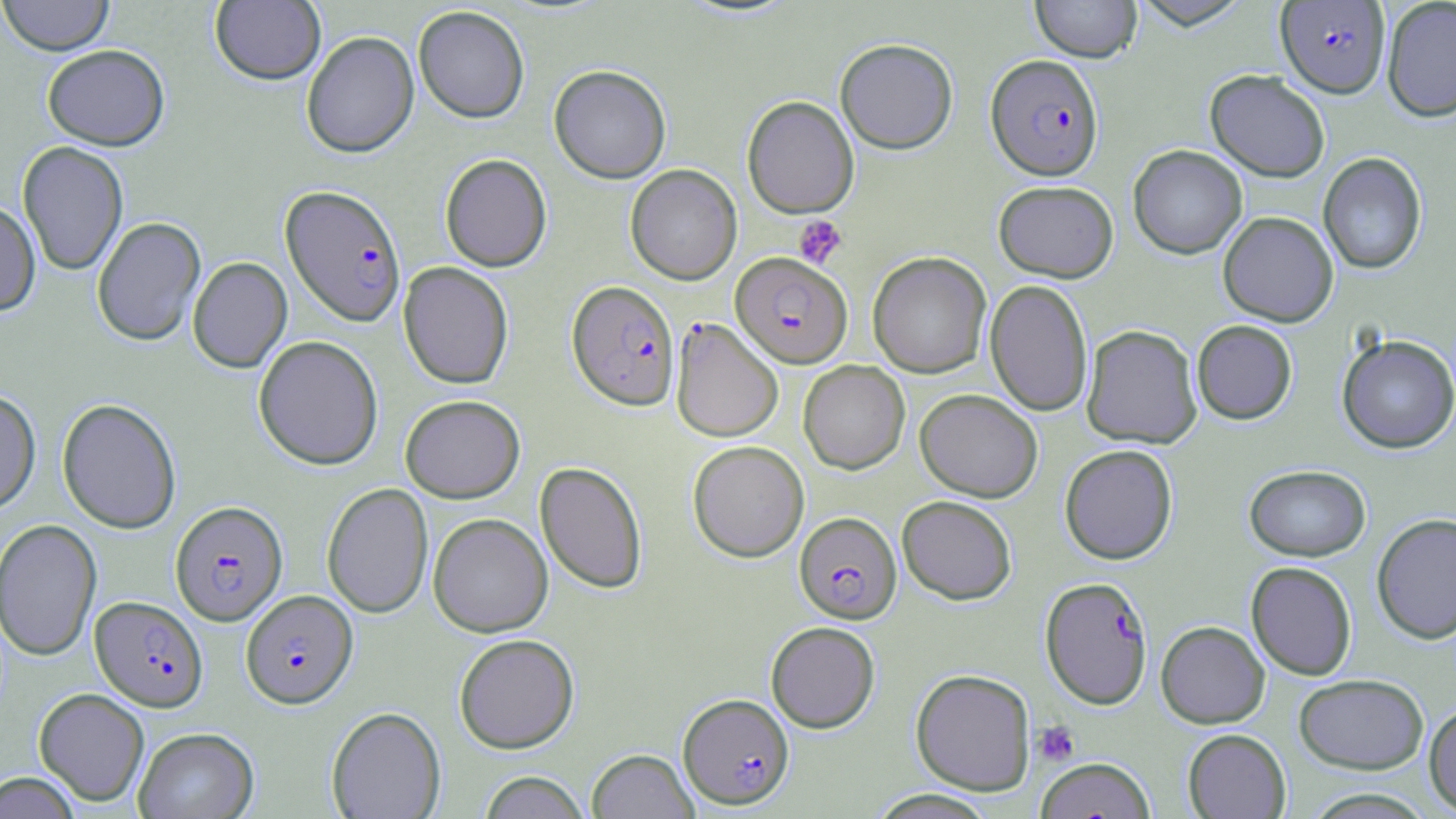

slide-level diagnosis = Plasmodium falciparum
platelet locations = approximate bounding boxes as (x1, y1, x2, y2) in pixels: (793, 215, 847, 267), (1032, 721, 1079, 766)
Plasmodium falciparum-infected red blood cell locations = approximate bounding boxes as (x1, y1, x2, y2) in pixels: (1275, 1, 1390, 97), (986, 54, 1103, 180), (280, 183, 407, 327), (731, 253, 852, 368), (567, 280, 679, 410), (666, 316, 782, 441), (170, 500, 288, 625), (795, 512, 901, 623), (1040, 576, 1152, 708), (241, 590, 357, 708), (90, 596, 207, 711), (679, 693, 794, 809)
field of view = single
uninfected red blood cell locations = approximate bounding boxes as (x1, y1, x2, y2) in pixels: (0, 0, 115, 57), (210, 0, 326, 85), (1030, 0, 1142, 62), (1130, 0, 1253, 29), (1381, 0, 1456, 122), (413, 5, 530, 123), (301, 31, 419, 158), (835, 38, 958, 154), (42, 44, 169, 150), (549, 65, 671, 183), (1205, 69, 1330, 183), (741, 95, 859, 218), (17, 141, 128, 275), (1128, 144, 1247, 259), (1318, 152, 1427, 274), (440, 153, 551, 272), (625, 164, 742, 284), (994, 180, 1118, 282), (0, 200, 40, 316), (1218, 211, 1338, 327), (92, 216, 205, 346), (867, 252, 991, 378), (187, 256, 292, 373), (398, 262, 514, 389), (985, 279, 1093, 417), (1191, 320, 1297, 425), (1081, 324, 1202, 448), (1336, 334, 1456, 454), (253, 335, 383, 470), (798, 361, 910, 474), (915, 388, 1042, 502), (0, 389, 40, 515), (400, 394, 525, 502), (57, 398, 182, 534), (688, 440, 809, 562), (1060, 444, 1178, 564), (535, 461, 648, 593), (1244, 464, 1370, 561), (321, 483, 433, 618), (897, 495, 1017, 604), (1371, 512, 1456, 645), (428, 513, 553, 637), (1, 518, 102, 661), (1245, 561, 1357, 680), (766, 621, 880, 732), (1156, 621, 1270, 728), (454, 633, 579, 753), (910, 668, 1035, 795), (1294, 673, 1429, 774), (34, 687, 149, 806), (1423, 701, 1456, 814), (326, 706, 446, 819), (133, 727, 259, 819), (1183, 729, 1291, 818), (587, 748, 698, 819), (1036, 757, 1156, 819), (0, 771, 82, 818), (477, 771, 591, 818), (1299, 788, 1439, 818), (866, 789, 1000, 818)
image size = 1456×819 pixels
stain = May-Grünwald-Giemsa
modality = optical microscopy
magnification = 1000x
preparation = thin blood smear